Draw a bounding box around every Plasmodium parasite, every leukocyte, and every artifact (stain precipitate or debris).
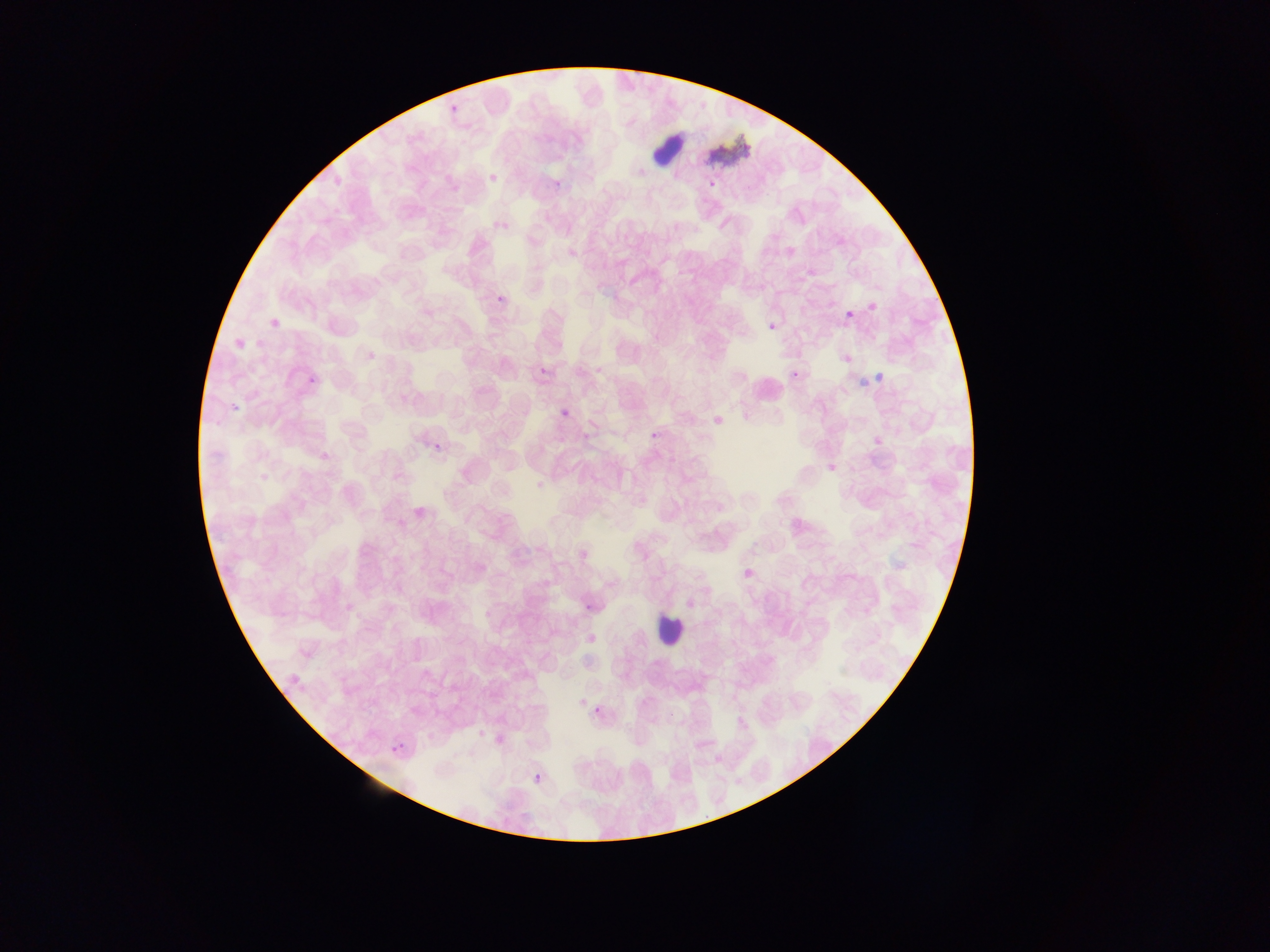

Approximate bounding boxes as left top right bottom in pixels.
Plasmodium parasites: 488 172 499 183; 707 180 716 190; 496 221 508 231; 845 309 856 319; 767 322 776 331; 538 366 548 375; 560 408 569 417; 433 443 443 452; 584 603 593 611.
Leukocytes: 652 129 688 170; 492 289 508 302; 269 316 278 330; 788 368 801 380; 307 376 321 386; 229 400 241 413; 648 429 658 447; 654 612 686 645; 593 702 604 717; 391 741 406 756; 532 773 542 785.
Artifacts (stain precipitate or debris): 703 132 751 175.

Collected in Ghana. Mobile-phone photograph taken through the microscope. Image is 1270×952 pixels. One field of view. Thin blood film.